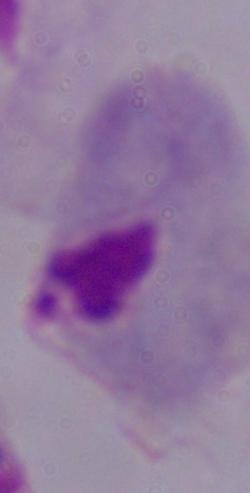

Summary:
  - Identification: trichomonad
  - Modality: micrograph
  - Magnification: 1000x